Locate every Plasmodium parasite.
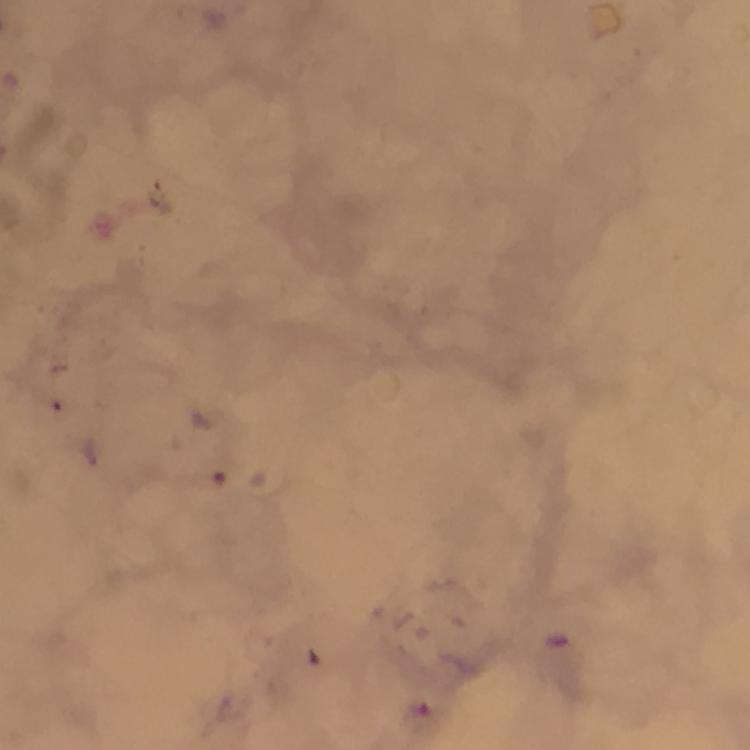
Approximate centers as (x, y) in pixels.
Plasmodium parasites: (421, 719).

Photographed through the microscope with a smartphone camera. Thick blood film. Cropped region of a single field of view. 100x magnification. Immersion oil was used. Giemsa stain. From a malaria diagnostic workup. Image is 750×750 pixels.